Name the cell type shown.
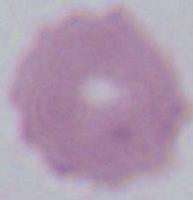

This is an erythrocyte.

1000x magnification. Micrograph.